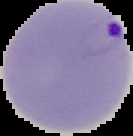
result = malaria parasites detected
image size = 133×136 pixels
image type = segmented cell region with the area outside set to black
preparation = thin blood smear